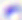

magnification = 400x
modality = photomicrograph
identification = Toxoplasma gondii